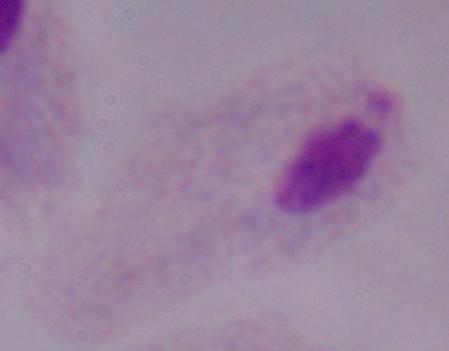

A trichomonad is shown. Captured at 1000x magnification. Photomicrograph.